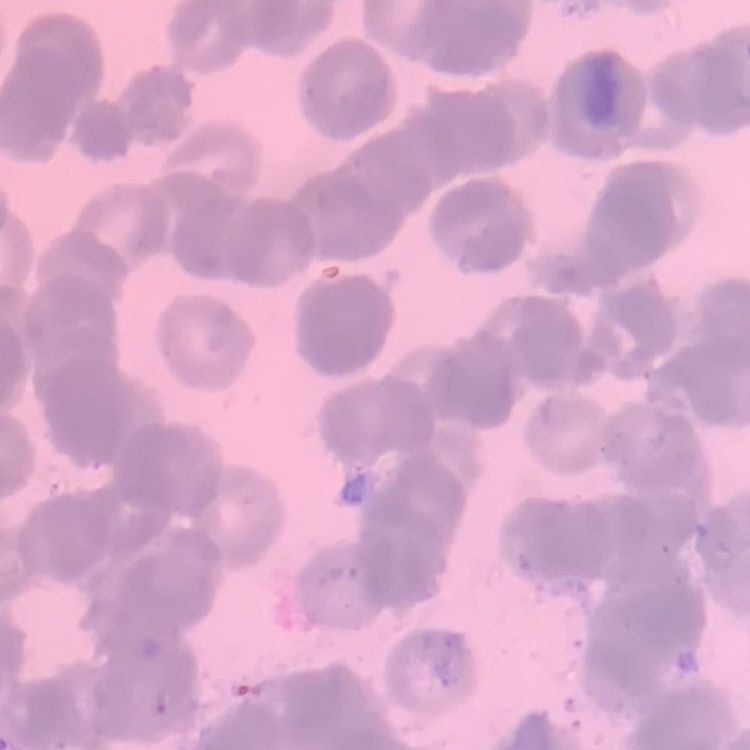

Summary:
  - Erythrocyte morphology: rouleaux formation
  - Image type: one tile cut from a larger photomicrograph
  - Stain: Field's or Giemsa
  - Preparation: thin blood smear